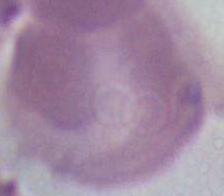

An erythrocyte is seen. Captured at 1000x magnification. Micrograph.